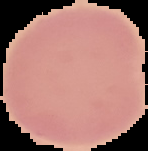

{
  "result": "no malaria parasites detected",
  "image_type": "cell region segmented out of the field of view; surrounding area masked to black",
  "image_size": "148×151 pixels",
  "preparation": "thin blood film"
}